Locate every Plasmodium falciparum-infected red blood cell.
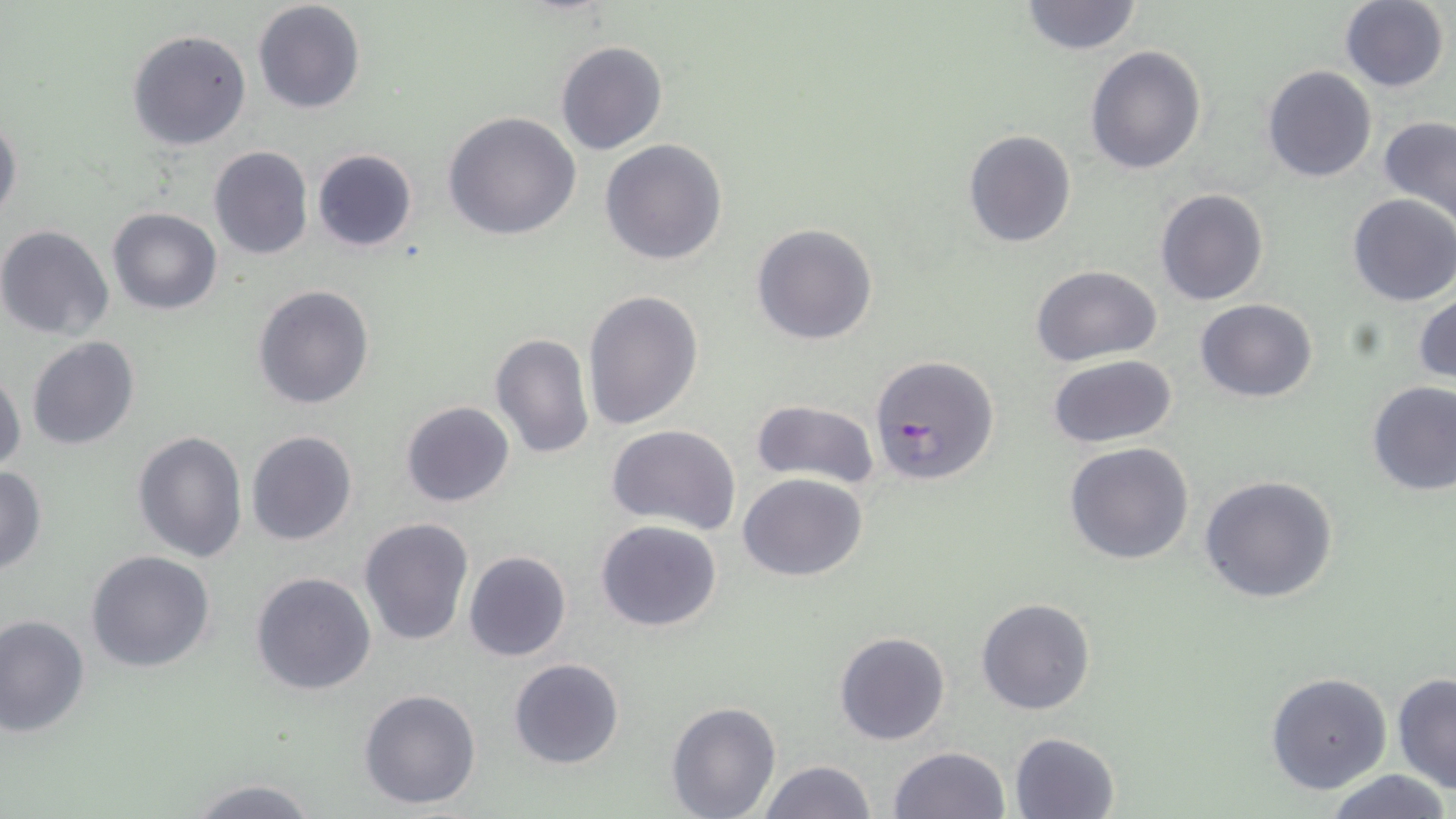
Approximate bounding boxes as named x1/y1/x2/y2 corners in pixels.
Plasmodium falciparum-infected red blood cells: (x1=871, y1=355, x2=1001, y2=486).

Summary:
  - Uninfected red blood cell locations: (x1=1019, y1=0, x2=1144, y2=55), (x1=1339, y1=0, x2=1450, y2=91), (x1=252, y1=1, x2=368, y2=115), (x1=126, y1=28, x2=252, y2=151), (x1=555, y1=39, x2=668, y2=155), (x1=1085, y1=44, x2=1207, y2=175), (x1=1262, y1=65, x2=1379, y2=183), (x1=443, y1=112, x2=582, y2=242), (x1=0, y1=115, x2=23, y2=226), (x1=1378, y1=115, x2=1456, y2=228), (x1=962, y1=129, x2=1077, y2=249), (x1=599, y1=138, x2=729, y2=266), (x1=207, y1=145, x2=314, y2=261), (x1=312, y1=148, x2=419, y2=253), (x1=1155, y1=189, x2=1269, y2=307), (x1=1348, y1=193, x2=1456, y2=306), (x1=106, y1=207, x2=222, y2=315), (x1=751, y1=223, x2=879, y2=346), (x1=0, y1=224, x2=114, y2=341), (x1=1030, y1=264, x2=1163, y2=365), (x1=252, y1=283, x2=376, y2=410), (x1=583, y1=290, x2=703, y2=433), (x1=1413, y1=294, x2=1456, y2=385), (x1=1196, y1=299, x2=1318, y2=402), (x1=488, y1=331, x2=594, y2=461), (x1=26, y1=337, x2=141, y2=452), (x1=1049, y1=355, x2=1178, y2=449), (x1=0, y1=365, x2=25, y2=475), (x1=1367, y1=380, x2=1456, y2=495), (x1=748, y1=399, x2=881, y2=489), (x1=400, y1=401, x2=516, y2=508), (x1=607, y1=424, x2=741, y2=531), (x1=132, y1=430, x2=247, y2=562), (x1=245, y1=430, x2=359, y2=546), (x1=1064, y1=442, x2=1195, y2=565), (x1=0, y1=465, x2=49, y2=575), (x1=739, y1=472, x2=869, y2=582), (x1=1199, y1=476, x2=1339, y2=605), (x1=358, y1=517, x2=473, y2=647), (x1=596, y1=519, x2=723, y2=633), (x1=85, y1=550, x2=215, y2=674), (x1=463, y1=551, x2=571, y2=662), (x1=250, y1=570, x2=378, y2=697), (x1=976, y1=598, x2=1096, y2=715), (x1=0, y1=615, x2=90, y2=738), (x1=834, y1=631, x2=952, y2=746), (x1=508, y1=658, x2=626, y2=770), (x1=1266, y1=672, x2=1393, y2=794), (x1=1392, y1=673, x2=1456, y2=794), (x1=359, y1=687, x2=482, y2=810), (x1=666, y1=701, x2=780, y2=819), (x1=1010, y1=731, x2=1121, y2=819), (x1=888, y1=746, x2=1011, y2=819), (x1=756, y1=759, x2=875, y2=819), (x1=1325, y1=769, x2=1451, y2=819), (x1=184, y1=777, x2=323, y2=819)
  - Slide-level diagnosis: Plasmodium falciparum
  - Image size: 1456×819 pixels
  - Preparation: thin blood smear
  - Modality: optical microscopy
  - Stain: May-Grünwald-Giemsa
  - Magnification: 1000x
  - Field of view: single